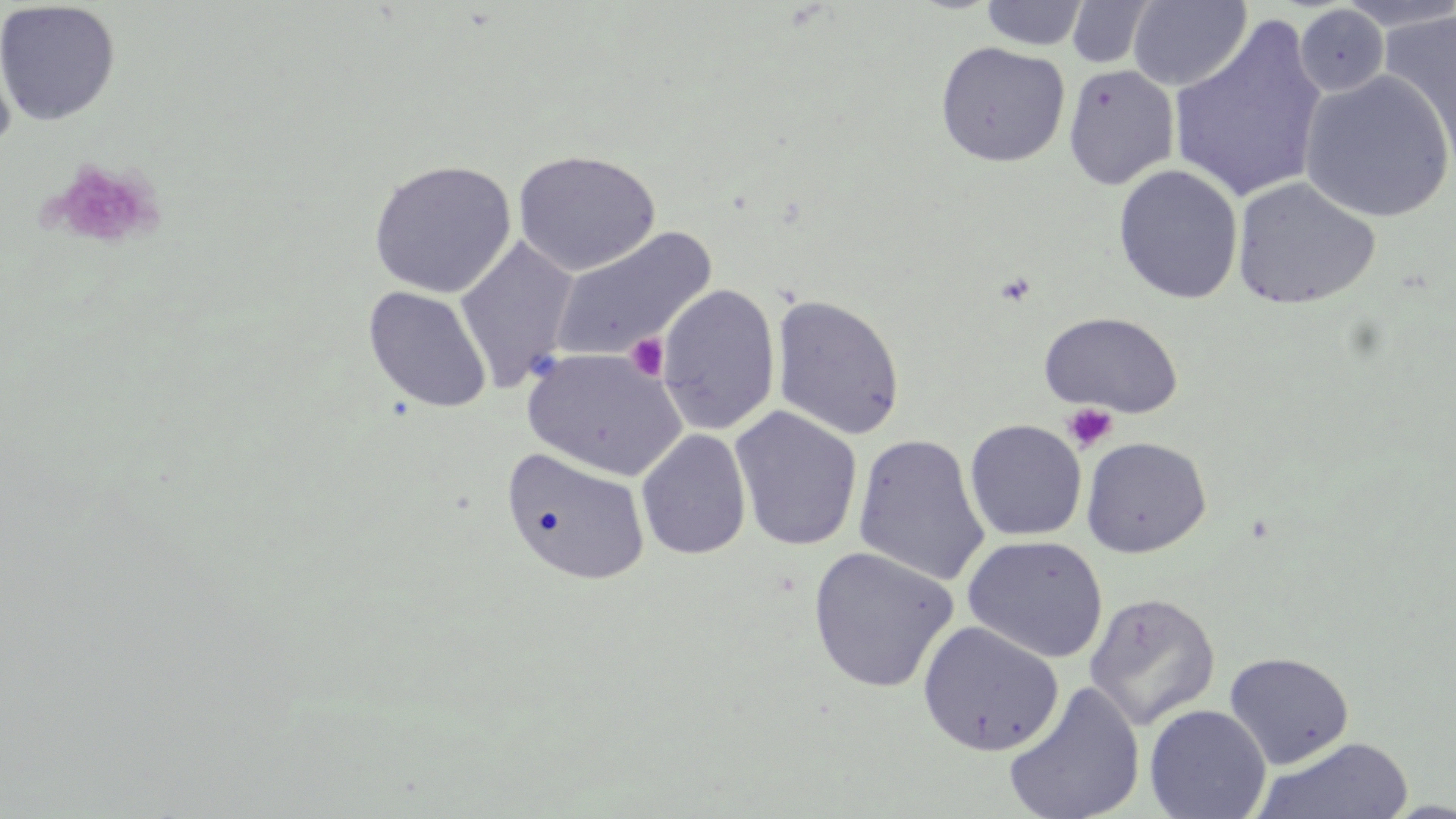
{
  "slide_level_diagnosis": "no evidence of blood parasites",
  "platelet_locations": "approximate bounding boxes as (x1, y1, x2, y2) in pixels: (49, 159, 162, 250), (625, 333, 671, 381), (1062, 402, 1119, 453)",
  "uninfected_red_blood_cell_locations": "approximate bounding boxes as (x1, y1, x2, y2) in pixels: (979, 0, 1090, 50), (1127, 0, 1252, 91), (1065, 1, 1157, 69), (1336, 1, 1454, 33), (0, 2, 121, 126), (1293, 5, 1389, 96), (1379, 7, 1455, 171), (1168, 16, 1329, 205), (935, 41, 1071, 167), (1063, 64, 1180, 190), (1298, 70, 1455, 223), (513, 149, 661, 277), (368, 159, 516, 299), (1113, 164, 1244, 304), (1232, 177, 1381, 310), (550, 227, 717, 363), (454, 236, 580, 391), (656, 283, 781, 436), (363, 286, 492, 414), (771, 294, 906, 441), (1039, 311, 1183, 418), (523, 347, 687, 482), (729, 406, 863, 551), (964, 419, 1087, 542), (636, 429, 752, 561), (852, 433, 990, 586), (1080, 436, 1212, 558), (500, 447, 651, 586), (962, 535, 1109, 663), (807, 546, 959, 694), (941, 569, 1094, 734), (1084, 592, 1221, 730), (916, 621, 1064, 756), (1224, 651, 1354, 770), (1002, 682, 1145, 819), (1144, 704, 1272, 819), (1255, 736, 1415, 819)",
  "image_size": "1456×819 pixels",
  "stain": "May-Grünwald-Giemsa",
  "preparation": "thin blood film",
  "magnification": "1000x",
  "field_of_view": "one of a larger specimen",
  "modality": "optical microscopy"
}